Locate every blood parasite and identify its species.
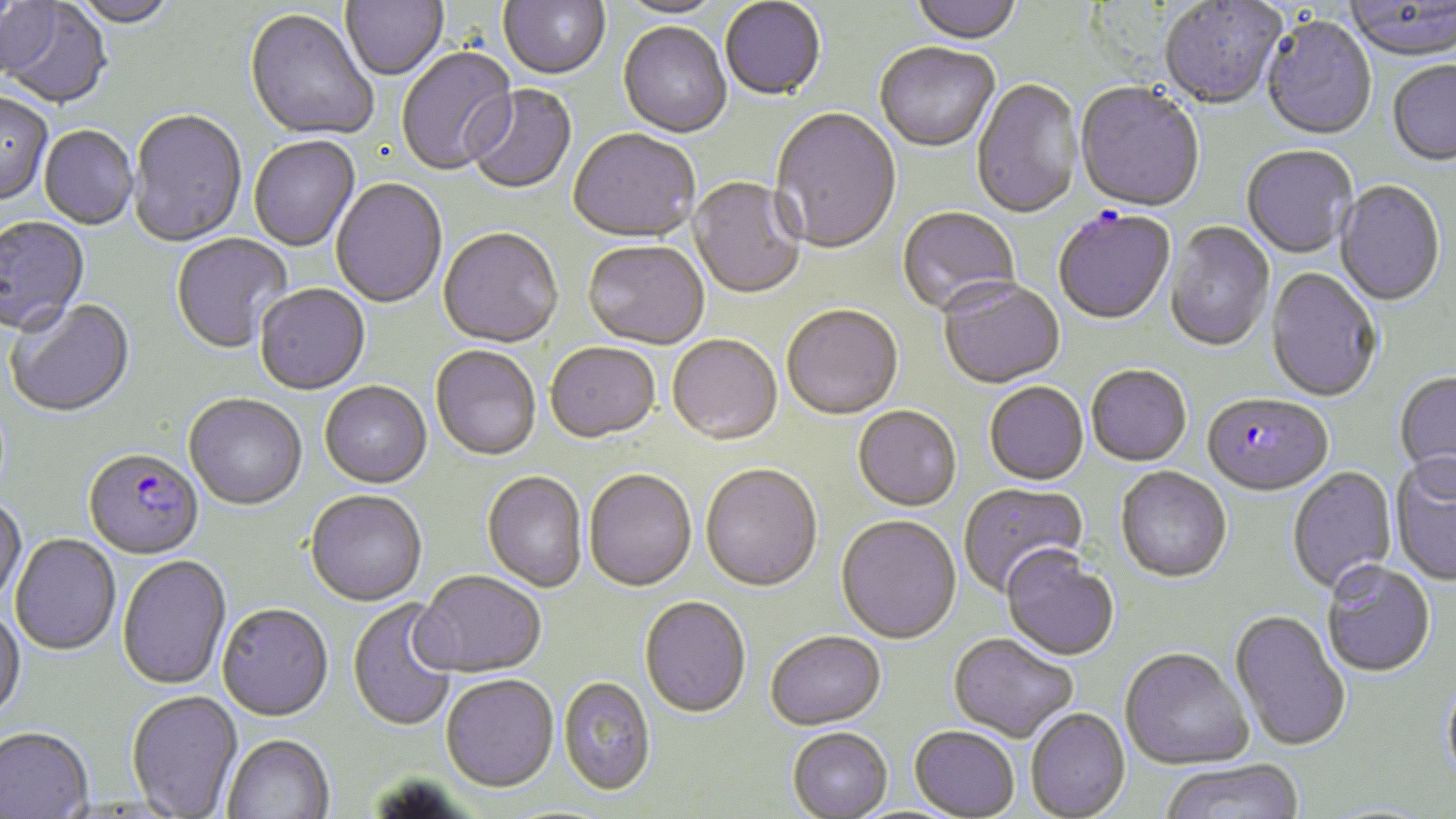

Approximate bounding boxes as [x1, y1, x2, y2] in pixels.
Plasmodium falciparum-infected red blood cells (subset): [1202, 395, 1333, 499], [85, 451, 204, 561].
No Plasmodium ovale, Plasmodium malariae, Plasmodium vivax, Babesia divergens, or Trypanosoma brucei observed.

Summary:
  - Uninfected red blood cell locations (subset): [68, 0, 178, 30], [341, 0, 448, 82], [498, 0, 610, 82], [910, 0, 1021, 46], [1, 1, 60, 81], [616, 1, 728, 20], [720, 1, 826, 103], [1160, 1, 1286, 111], [1343, 1, 1456, 64], [0, 2, 112, 109], [244, 11, 378, 142], [1260, 18, 1377, 142], [618, 23, 731, 139], [875, 45, 1000, 154], [397, 48, 517, 177], [1387, 62, 1456, 167], [971, 79, 1083, 221], [466, 84, 577, 196], [1075, 84, 1204, 214], [0, 94, 53, 207], [769, 108, 902, 257], [128, 111, 247, 248], [39, 127, 138, 231], [568, 131, 700, 245], [249, 136, 360, 252], [1242, 147, 1358, 260], [688, 177, 806, 301], [331, 179, 447, 309], [1335, 182, 1445, 308], [898, 207, 1021, 318], [0, 217, 90, 338], [1164, 223, 1274, 354], [438, 230, 563, 350], [170, 233, 293, 355], [583, 242, 709, 351], [1265, 269, 1382, 403], [938, 281, 1065, 391], [254, 285, 370, 396], [6, 299, 135, 419], [782, 307, 903, 421], [667, 336, 782, 447], [546, 344, 661, 445], [431, 347, 541, 462], [1086, 367, 1192, 468], [1393, 372, 1456, 494], [319, 383, 432, 490], [984, 383, 1089, 487], [184, 396, 307, 511], [852, 408, 962, 513], [1390, 458, 1456, 587], [700, 466, 823, 594], [1287, 467, 1398, 595], [1115, 468, 1232, 585], [584, 471, 697, 593], [482, 472, 588, 593], [958, 483, 1089, 598], [305, 492, 427, 608], [0, 496, 27, 608], [835, 517, 961, 646], [10, 534, 120, 656], [1001, 550, 1120, 662], [118, 556, 232, 691], [1322, 563, 1436, 679], [412, 572, 546, 680], [640, 598, 751, 720], [347, 599, 459, 733], [217, 606, 334, 724], [0, 609, 26, 724], [1229, 610, 1350, 753], [766, 633, 887, 732], [949, 634, 1078, 743], [1120, 649, 1254, 771], [1440, 671, 1456, 795], [440, 677, 559, 795], [558, 678, 656, 798], [126, 691, 243, 818], [1026, 708, 1131, 818], [909, 727, 1020, 819], [0, 728, 94, 819], [787, 729, 893, 818], [222, 736, 335, 819], [1159, 760, 1306, 819]
  - Slide-level diagnosis: Plasmodium falciparum
  - Preparation: thin blood film
  - Magnification: 1000x
  - Stain: May-Grünwald-Giemsa
  - Image size: 1456×819 pixels
  - Field of view: one of a larger specimen
  - Modality: light microscopy